Comment on the morphology of the erythrocytes.
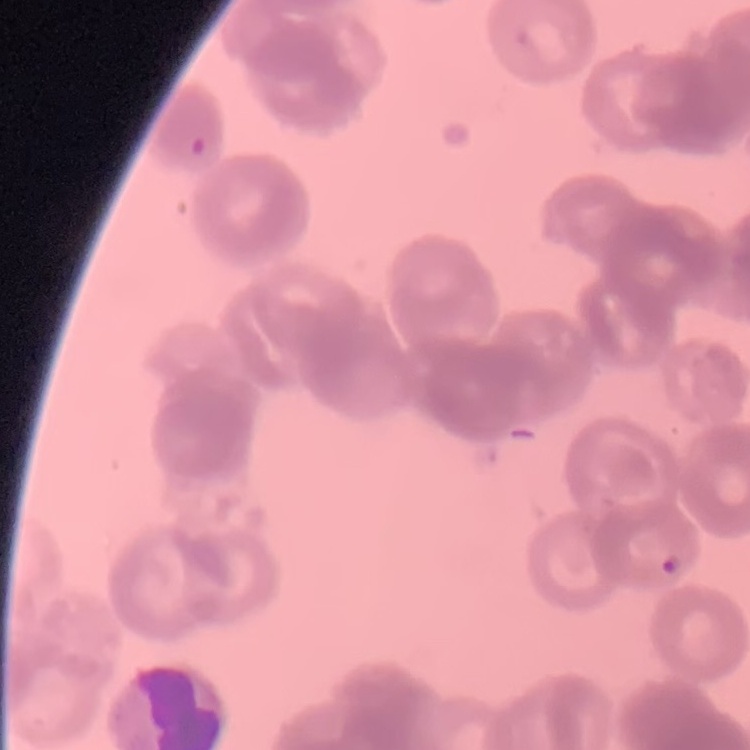

They show rouleaux formation.

{
  "image_type": "one tile cut from a larger photomicrograph",
  "preparation": "thin blood smear",
  "stain": "Field's or Giemsa"
}